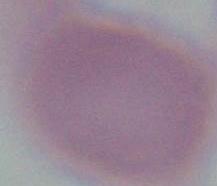
Summary:
  - Identification: erythrocyte
  - Modality: photomicrograph
  - Magnification: 1000x